Locate the cells, classifying each as a parasitized RBC, an uninfected RBC, or a WBC.
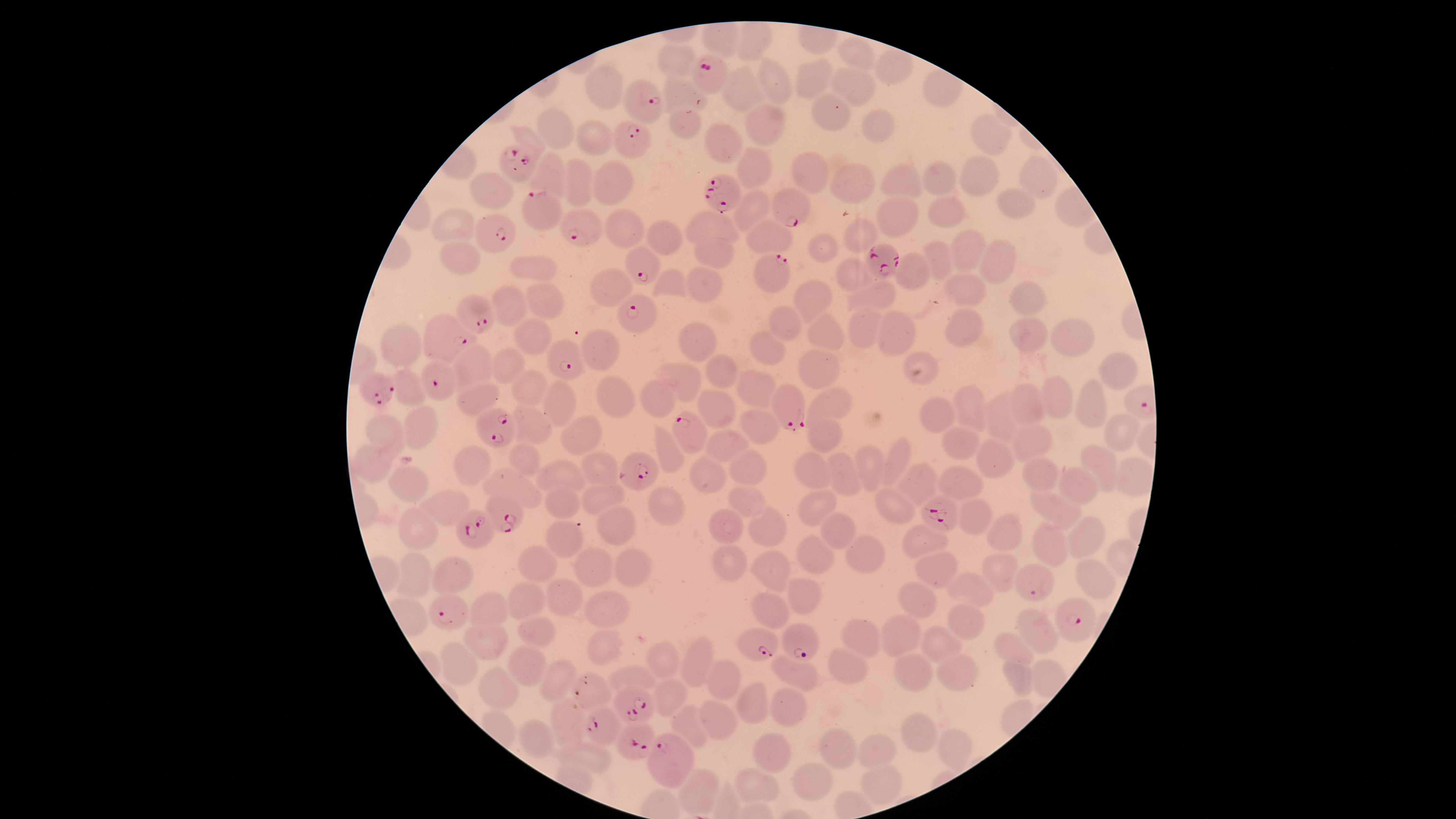

Approximate marker points, in pixels from the top-left corner.
Parasitized RBCs: (x=711, y=73), (x=643, y=88), (x=632, y=145), (x=516, y=170), (x=728, y=188), (x=788, y=205), (x=544, y=214), (x=583, y=224), (x=489, y=227), (x=883, y=257), (x=639, y=261), (x=774, y=268), (x=477, y=310), (x=641, y=320), (x=444, y=334), (x=563, y=350), (x=444, y=377), (x=374, y=381), (x=792, y=405), (x=487, y=420), (x=690, y=433), (x=634, y=464), (x=945, y=507), (x=499, y=508), (x=479, y=529), (x=1032, y=579), (x=448, y=605), (x=1071, y=608), (x=801, y=637), (x=755, y=641), (x=594, y=686), (x=633, y=693), (x=609, y=720), (x=640, y=733), (x=669, y=755).
Uninfected RBCs: (x=857, y=52), (x=892, y=70), (x=814, y=74), (x=769, y=81), (x=850, y=83), (x=601, y=85), (x=744, y=91), (x=828, y=118), (x=766, y=119), (x=876, y=121), (x=554, y=128), (x=588, y=135), (x=995, y=135), (x=528, y=136), (x=723, y=141), (x=755, y=165), (x=1037, y=171), (x=806, y=172), (x=851, y=176), (x=905, y=177), (x=947, y=178), (x=547, y=179), (x=983, y=179), (x=609, y=180), (x=578, y=183), (x=487, y=195), (x=752, y=204), (x=1020, y=204), (x=900, y=210), (x=940, y=211), (x=458, y=222), (x=709, y=225), (x=625, y=228), (x=855, y=232), (x=771, y=235), (x=664, y=237), (x=818, y=244), (x=713, y=250), (x=459, y=251), (x=969, y=252), (x=939, y=259), (x=1000, y=262), (x=536, y=269), (x=849, y=270), (x=913, y=270), (x=705, y=280), (x=674, y=285), (x=961, y=285), (x=606, y=291), (x=815, y=292), (x=877, y=294), (x=544, y=297), (x=1023, y=298), (x=513, y=308), (x=790, y=320), (x=964, y=323), (x=863, y=326), (x=902, y=327), (x=823, y=331), (x=532, y=334), (x=1068, y=335), (x=1024, y=337), (x=766, y=339), (x=697, y=340), (x=595, y=346), (x=401, y=349), (x=817, y=359), (x=476, y=361), (x=1117, y=368), (x=717, y=371), (x=923, y=372), (x=509, y=373), (x=683, y=382), (x=747, y=383), (x=410, y=389), (x=612, y=391), (x=479, y=393), (x=527, y=396), (x=660, y=397), (x=564, y=398), (x=1060, y=400), (x=841, y=401), (x=1031, y=402), (x=973, y=406), (x=1087, y=407), (x=714, y=409), (x=939, y=410), (x=1002, y=416), (x=424, y=420), (x=530, y=423), (x=754, y=423), (x=384, y=425), (x=584, y=430), (x=1113, y=430), (x=823, y=436), (x=1035, y=441), (x=965, y=443), (x=732, y=445), (x=669, y=450), (x=529, y=457), (x=1100, y=458), (x=896, y=460), (x=990, y=461), (x=471, y=462), (x=368, y=463), (x=871, y=465), (x=743, y=466), (x=601, y=469), (x=816, y=471), (x=565, y=474), (x=1040, y=474), (x=707, y=475), (x=950, y=477), (x=1130, y=477), (x=914, y=479), (x=847, y=480), (x=412, y=483), (x=511, y=483), (x=1086, y=487), (x=599, y=491), (x=749, y=497), (x=561, y=502), (x=665, y=504), (x=447, y=505), (x=818, y=505), (x=889, y=505), (x=1052, y=507), (x=973, y=518), (x=412, y=525), (x=725, y=528), (x=839, y=528), (x=623, y=530), (x=770, y=532), (x=1000, y=534), (x=1088, y=537), (x=917, y=538), (x=567, y=540), (x=1052, y=544), (x=863, y=549), (x=809, y=555), (x=728, y=558), (x=630, y=561), (x=597, y=567), (x=933, y=568), (x=541, y=570), (x=995, y=570), (x=419, y=573), (x=454, y=573), (x=773, y=573), (x=1096, y=577), (x=976, y=590), (x=805, y=596), (x=566, y=599), (x=914, y=599), (x=527, y=601), (x=605, y=602), (x=769, y=606), (x=496, y=607), (x=969, y=625), (x=539, y=628), (x=1038, y=631), (x=903, y=636), (x=861, y=637), (x=488, y=641), (x=597, y=643), (x=942, y=644), (x=1018, y=651), (x=692, y=661), (x=666, y=662), (x=522, y=663), (x=461, y=664), (x=850, y=665), (x=959, y=672), (x=636, y=675), (x=802, y=675), (x=1016, y=675), (x=556, y=677), (x=916, y=677), (x=725, y=685), (x=498, y=688), (x=673, y=701), (x=748, y=703), (x=784, y=703), (x=566, y=716), (x=713, y=721), (x=920, y=730), (x=694, y=731), (x=536, y=738), (x=940, y=745), (x=830, y=746), (x=881, y=749), (x=767, y=751), (x=588, y=755), (x=810, y=780), (x=757, y=782), (x=878, y=786), (x=695, y=792).
No WBCs identified.

capture = smartphone photograph through the microscope eyepiece
field of view = single
species = Plasmodium falciparum
preparation = thin blood film
image size = 1456×819 pixels
visible region = circular
stain = Giemsa